Assess this cell for malaria.
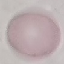
Uninfected.

Thin blood smear. Photographed with a smartphone camera at the microscope eyepiece. Cell patch, automatically extracted from a larger field of view and resized to 64 × 64 pixels. Giemsa-stained preparation.